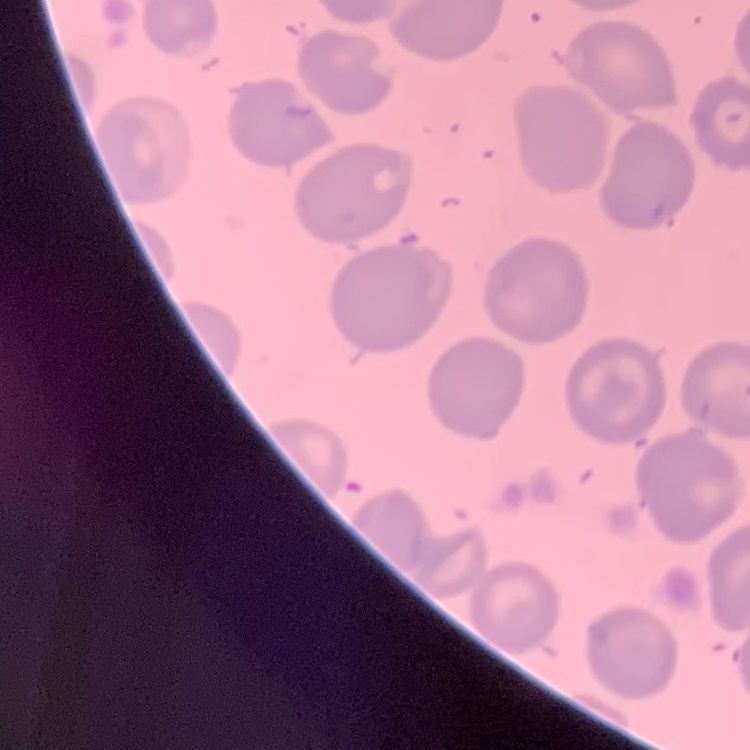
red blood cell morphology = no rouleaux formation
preparation = thin blood smear
image type = square crop of a larger photomicrograph
stain = Field's or Giemsa